Report the malaria status of this cell.
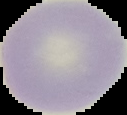

It is uninfected.

Image is 127×115 pixels. From a thin blood film. The area outside the segmented cell region is set to black.